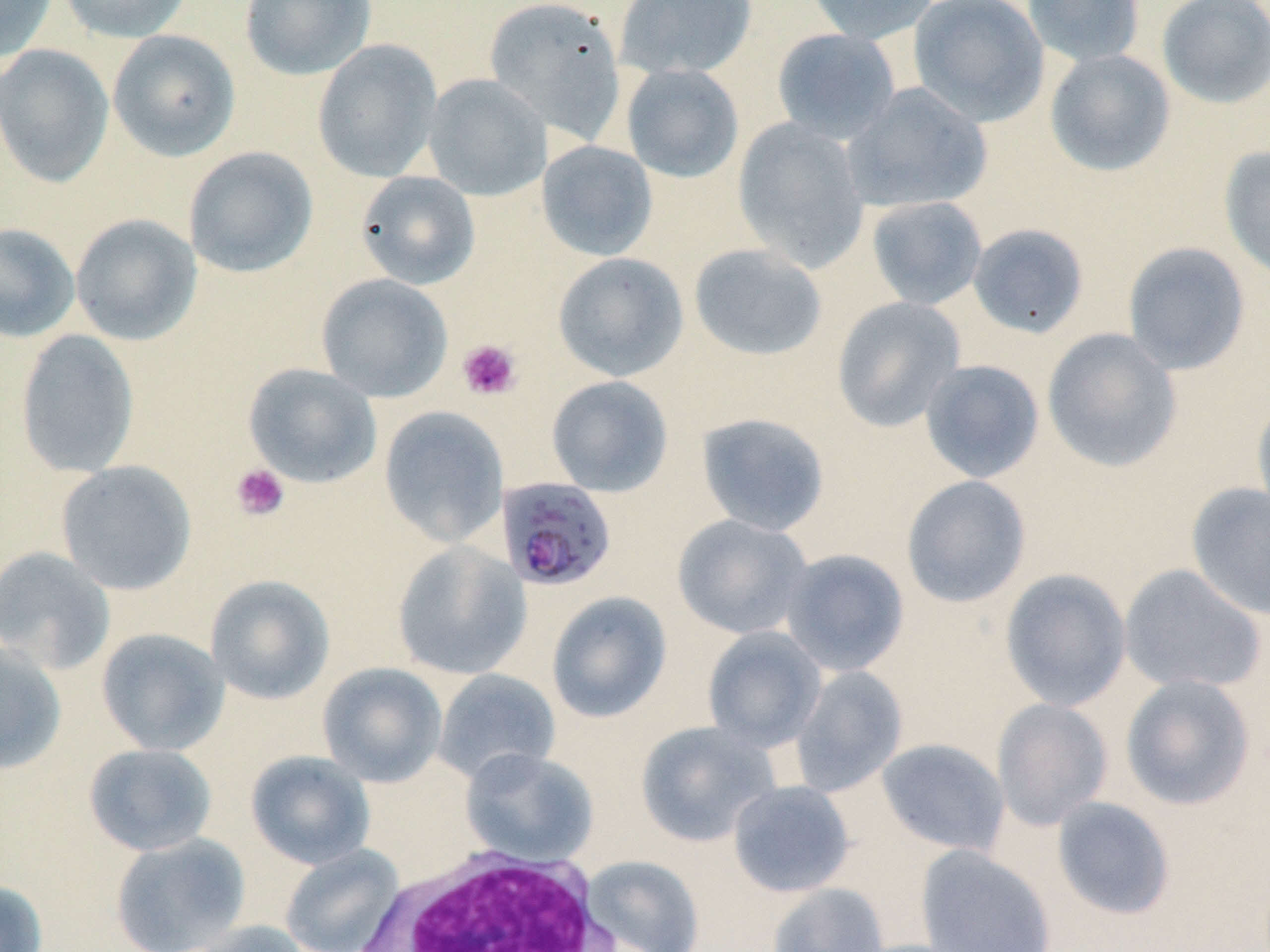 Approximate bounding boxes as [x1, y1, x2, y2] in pixels. Uninfected red blood cell locations: [0, 0, 58, 63], [58, 0, 192, 43], [239, 0, 376, 81], [484, 0, 626, 143], [615, 0, 758, 80], [805, 0, 939, 45], [908, 0, 1050, 127], [1022, 0, 1146, 68], [1156, 0, 1270, 109], [771, 28, 901, 144], [107, 29, 241, 161], [312, 39, 443, 183], [0, 43, 114, 187], [1044, 48, 1175, 177], [621, 63, 744, 183], [423, 73, 551, 201], [842, 82, 991, 214], [732, 118, 870, 273], [537, 140, 658, 261], [1219, 144, 1270, 283], [183, 146, 318, 278], [356, 171, 480, 289], [866, 196, 988, 310], [70, 213, 202, 346], [0, 222, 79, 343], [967, 223, 1089, 339], [1122, 242, 1251, 376], [688, 243, 828, 362], [552, 252, 689, 382], [316, 273, 453, 402], [831, 296, 966, 432], [1041, 327, 1183, 474], [15, 328, 140, 478], [919, 359, 1045, 483], [243, 363, 381, 488], [545, 375, 673, 497], [1251, 393, 1270, 525], [379, 405, 509, 547], [695, 412, 831, 536], [56, 461, 197, 596], [900, 475, 1032, 609], [1186, 482, 1270, 620], [672, 514, 813, 639], [391, 541, 531, 681], [0, 546, 116, 675], [779, 548, 910, 677], [1119, 563, 1266, 695], [999, 568, 1132, 711], [204, 574, 335, 705], [546, 591, 672, 723], [702, 626, 827, 752], [95, 628, 229, 756], [0, 641, 67, 775], [317, 662, 447, 787], [790, 665, 909, 797], [432, 669, 561, 785], [1120, 674, 1256, 811], [991, 698, 1113, 831], [635, 720, 780, 847], [876, 738, 1010, 856], [83, 743, 217, 856], [459, 747, 600, 867], [245, 751, 375, 870], [727, 780, 855, 897], [1051, 796, 1176, 920], [110, 833, 251, 952], [279, 844, 404, 952], [916, 845, 1057, 952], [582, 855, 704, 952], [0, 879, 48, 952], [768, 882, 890, 952], [187, 920, 315, 952]. Platelet locations: [456, 339, 522, 401], [231, 463, 290, 521]. White blood cell locations: [346, 847, 625, 952]. Plasmodium falciparum-infected red blood cell locations: [497, 477, 618, 592]. Slide-level diagnosis: Plasmodium falciparum. 1000x magnification. Thin blood film. Image is 1270×952 pixels. One field of a larger specimen. May-Grünwald-Giemsa-stained preparation. Optical microscopy.